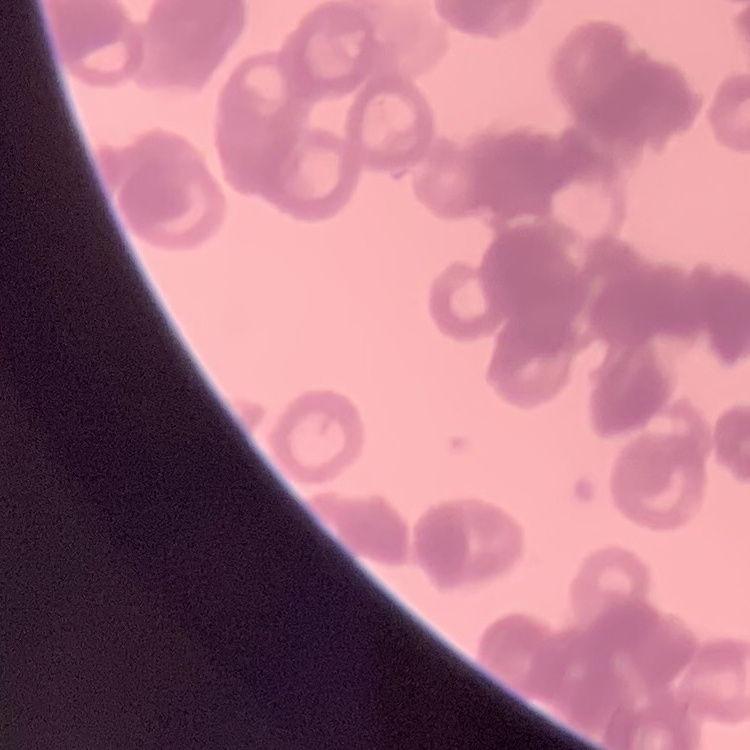
Summary:
  - Red blood cell morphology: rouleaux formation
  - Image type: one tile cut from a larger photomicrograph
  - Stain: Field's or Giemsa
  - Preparation: thin peripheral smear